Name the parasite shown.
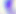

Toxoplasma gondii.

magnification = 400x
modality = micrograph